Give the extent of all uninfected red blood cells.
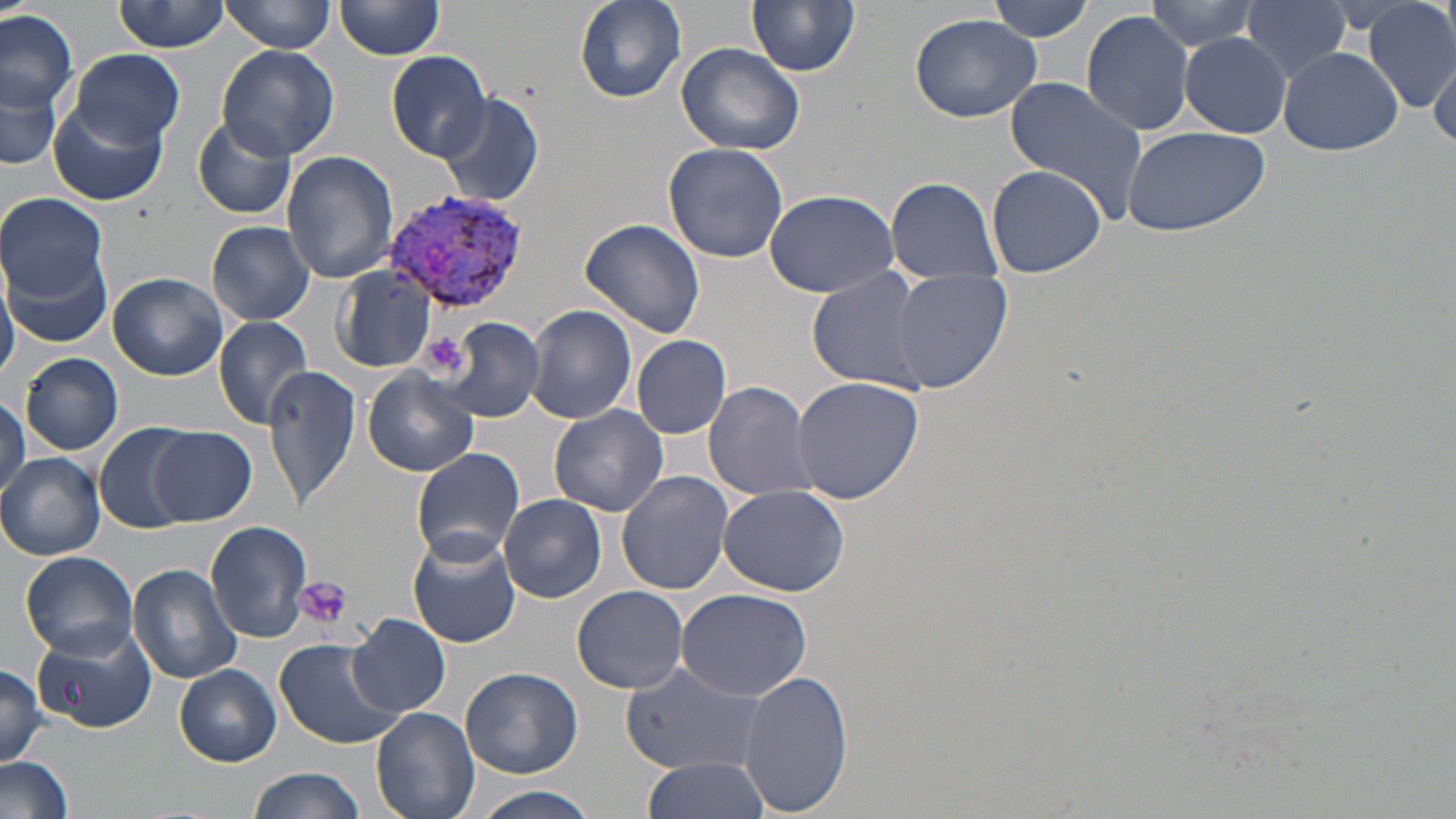

Approximate bounding boxes as named x1/y1/x2/y2 corners in pixels.
Uninfected red blood cells: (x1=221, y1=0, x2=337, y2=54), (x1=573, y1=0, x2=685, y2=102), (x1=747, y1=0, x2=860, y2=76), (x1=985, y1=0, x2=1099, y2=41), (x1=1144, y1=0, x2=1261, y2=53), (x1=114, y1=1, x2=230, y2=53), (x1=1240, y1=1, x2=1356, y2=85), (x1=334, y1=2, x2=445, y2=63), (x1=1364, y1=2, x2=1454, y2=114), (x1=0, y1=7, x2=79, y2=128), (x1=1082, y1=9, x2=1197, y2=136), (x1=909, y1=12, x2=1044, y2=122), (x1=1180, y1=33, x2=1290, y2=136), (x1=676, y1=42, x2=806, y2=155), (x1=216, y1=45, x2=342, y2=163), (x1=1278, y1=46, x2=1403, y2=156), (x1=70, y1=49, x2=185, y2=149), (x1=384, y1=50, x2=494, y2=162), (x1=1428, y1=56, x2=1456, y2=145), (x1=2, y1=74, x2=62, y2=173), (x1=1005, y1=76, x2=1149, y2=219), (x1=435, y1=94, x2=545, y2=209), (x1=49, y1=104, x2=168, y2=205), (x1=192, y1=115, x2=297, y2=220), (x1=1121, y1=126, x2=1272, y2=236), (x1=664, y1=141, x2=788, y2=263), (x1=282, y1=150, x2=398, y2=284), (x1=986, y1=165, x2=1106, y2=276), (x1=884, y1=177, x2=1006, y2=283), (x1=762, y1=188, x2=901, y2=297), (x1=1, y1=192, x2=108, y2=299), (x1=580, y1=218, x2=705, y2=338), (x1=209, y1=222, x2=316, y2=326), (x1=8, y1=255, x2=112, y2=348), (x1=807, y1=265, x2=933, y2=395), (x1=0, y1=266, x2=18, y2=384), (x1=333, y1=266, x2=436, y2=372), (x1=888, y1=269, x2=1013, y2=393), (x1=108, y1=272, x2=227, y2=380), (x1=521, y1=305, x2=638, y2=426), (x1=214, y1=316, x2=316, y2=429), (x1=440, y1=319, x2=544, y2=423), (x1=631, y1=334, x2=732, y2=440), (x1=20, y1=352, x2=123, y2=454), (x1=264, y1=364, x2=360, y2=511), (x1=362, y1=368, x2=478, y2=476), (x1=794, y1=377, x2=924, y2=504), (x1=703, y1=380, x2=816, y2=501), (x1=0, y1=396, x2=29, y2=501), (x1=550, y1=403, x2=669, y2=517), (x1=95, y1=423, x2=196, y2=533), (x1=149, y1=426, x2=257, y2=525), (x1=411, y1=447, x2=525, y2=562), (x1=0, y1=452, x2=106, y2=561), (x1=616, y1=469, x2=734, y2=595), (x1=718, y1=484, x2=849, y2=596), (x1=499, y1=494, x2=607, y2=603), (x1=205, y1=520, x2=314, y2=644), (x1=408, y1=532, x2=519, y2=649), (x1=19, y1=550, x2=140, y2=658), (x1=127, y1=564, x2=244, y2=685), (x1=571, y1=585, x2=689, y2=692), (x1=677, y1=588, x2=811, y2=701), (x1=349, y1=615, x2=451, y2=718), (x1=30, y1=626, x2=156, y2=729), (x1=272, y1=637, x2=402, y2=748), (x1=621, y1=661, x2=770, y2=775), (x1=174, y1=663, x2=281, y2=766), (x1=0, y1=664, x2=50, y2=766), (x1=460, y1=668, x2=585, y2=778), (x1=739, y1=668, x2=850, y2=817), (x1=371, y1=705, x2=481, y2=819), (x1=0, y1=755, x2=74, y2=819), (x1=639, y1=756, x2=770, y2=818), (x1=249, y1=767, x2=365, y2=819), (x1=463, y1=788, x2=606, y2=819).

Summary:
  - Platelet locations: (x1=421, y1=332, x2=468, y2=379), (x1=295, y1=574, x2=351, y2=629)
  - Plasmodium vivax-infected red blood cell locations: (x1=383, y1=187, x2=532, y2=319)
  - Slide-level diagnosis: Plasmodium vivax
  - Preparation: thin blood smear
  - Stain: May-Grünwald-Giemsa
  - Modality: optical microscopy
  - Image size: 1456×819 pixels
  - Field of view: one of a larger specimen
  - Magnification: 1000x